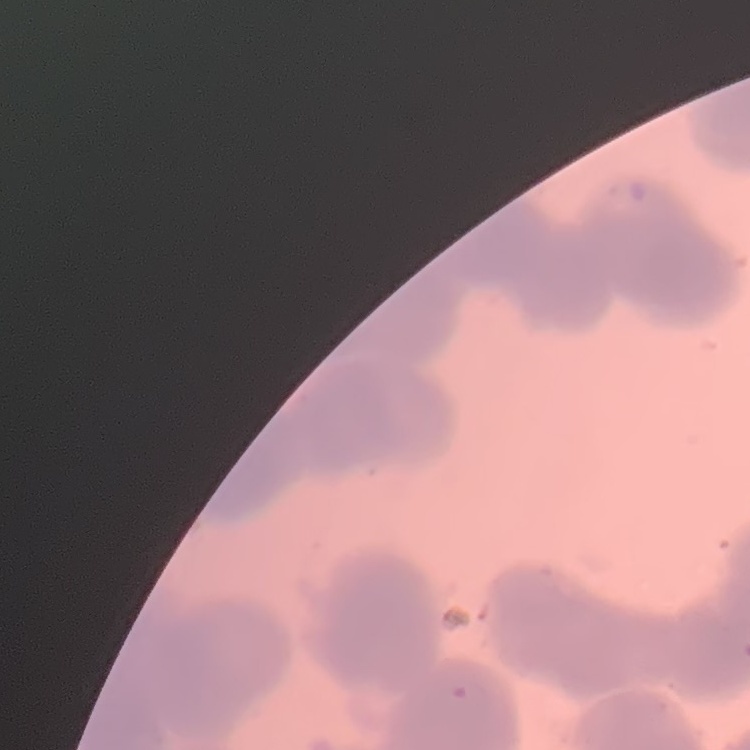

red_blood_cell_morphology: rouleaux formation
image_type: square crop of a larger photomicrograph
stain: Field's or Giemsa
preparation: thin blood smear